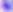 400x magnification. Micrograph. Toxoplasma gondii is shown.